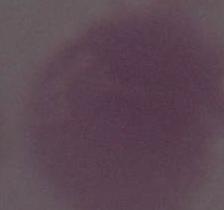 A red blood cell is seen. Photomicrograph. 1000x magnification.